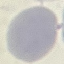

Summary:
  - Result: no malaria parasites detected
  - Image type: cell patch, automatically extracted from a larger field of view and resized to 64 × 64 pixels
  - Preparation: thin smear
  - Capture: smartphone camera at the microscope eyepiece
  - Stain: Giemsa